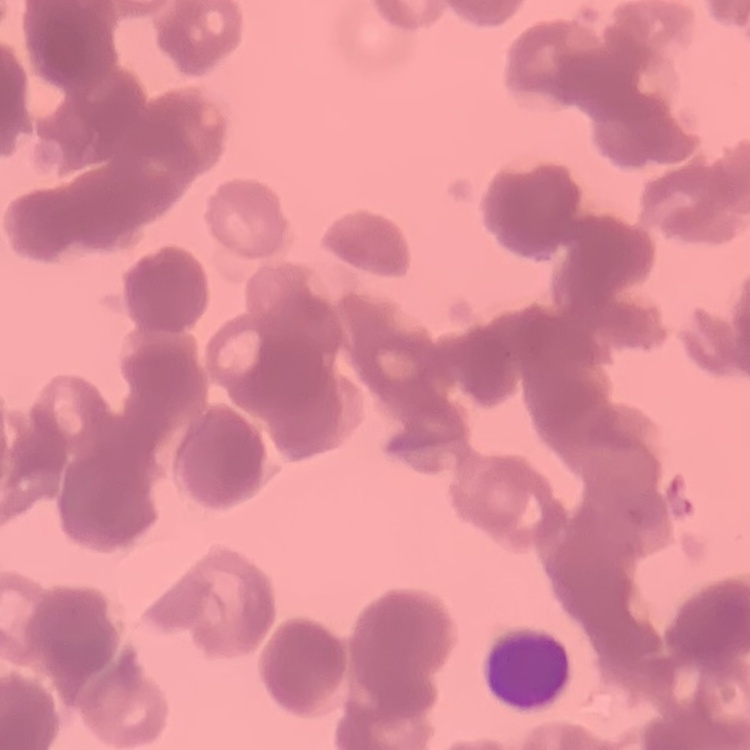
Summary:
  - Erythrocyte morphology: rouleaux formation
  - Stain: Field's or Giemsa
  - Image type: one tile cut from a larger photomicrograph
  - Preparation: thin blood smear